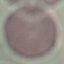
Result: no malaria parasites seen. Automatically extracted cell patch, resized to 64 × 64 pixels. Thin smear of blood. Giemsa stain. Photographed with a smartphone camera at the microscope eyepiece.